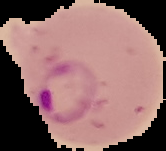
Summary:
  - Preparation: thin blood smear
  - Image type: cell region segmented out of the field of view; surrounding area masked to black
  - Image size: 166×151 pixels
  - Result: malaria parasites detected